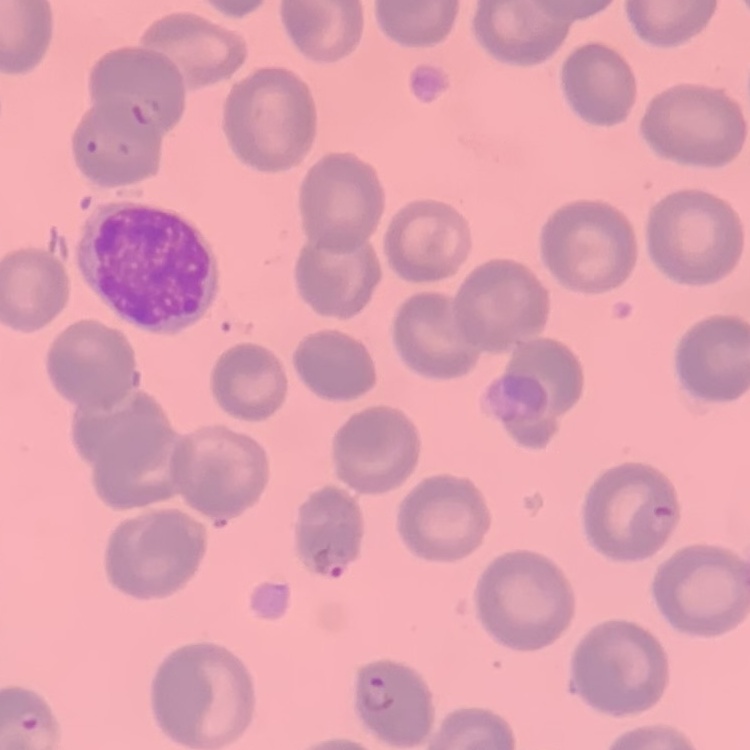

The erythrocytes exhibit no rouleaux formation. Stained with either Field's or Giemsa. Thin peripheral smear. Square crop of a larger photomicrograph.